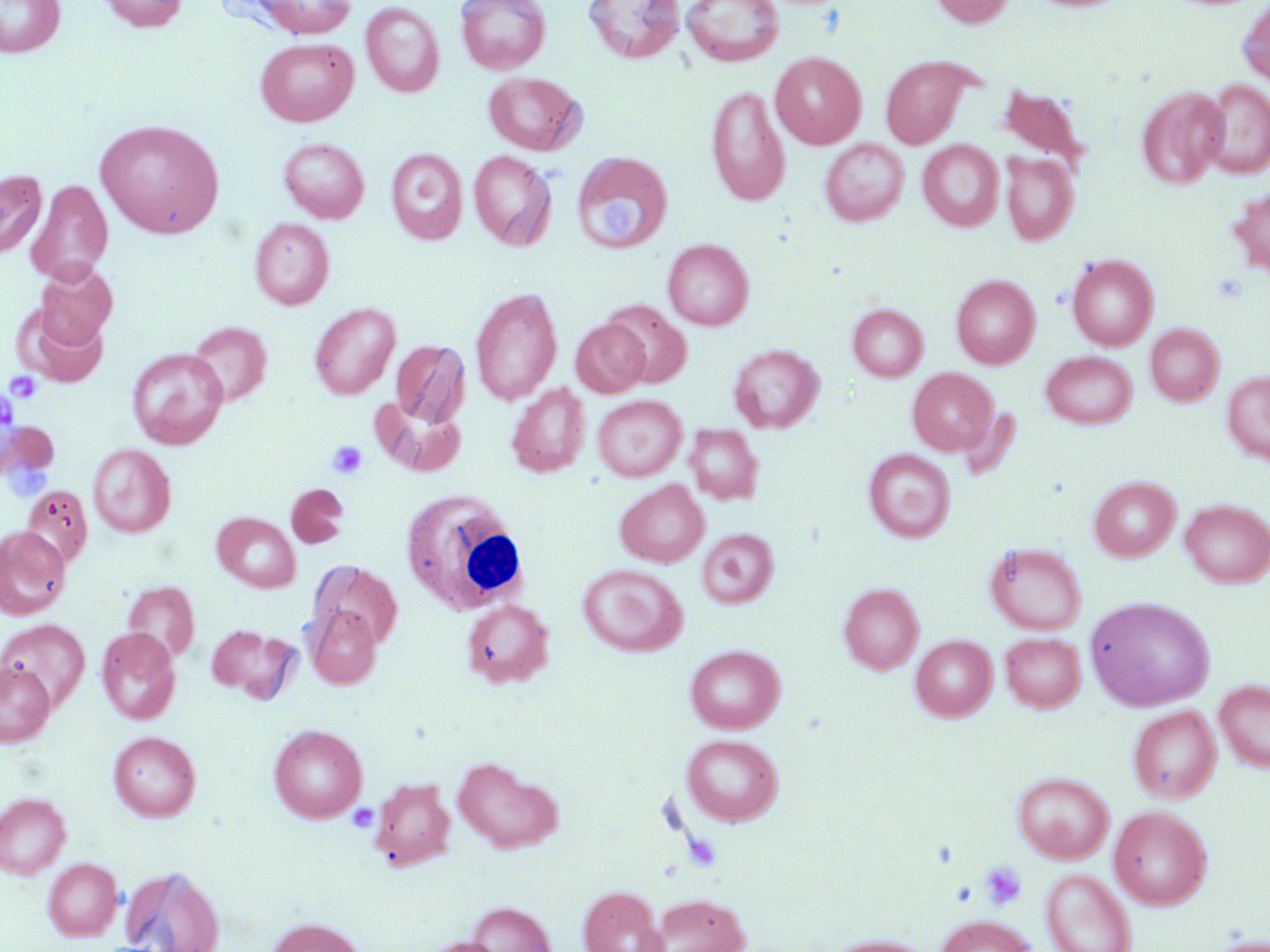
Approximate bounding boxes as (x1, y1, x2, y2) in pixels. Platelet locations (subset): (598, 195, 646, 243), (5, 371, 42, 405), (327, 440, 368, 479), (347, 804, 378, 832), (979, 862, 1026, 911), (950, 882, 976, 907). Uninfected red blood cell locations (subset): (0, 0, 65, 57), (100, 0, 187, 32), (456, 0, 550, 74), (583, 0, 685, 63), (682, 0, 784, 66), (929, 0, 1017, 28), (1029, 0, 1127, 13), (1238, 0, 1270, 90), (251, 1, 358, 38), (361, 1, 444, 97), (255, 38, 358, 126), (771, 51, 866, 149), (881, 54, 976, 149), (482, 71, 586, 155), (1200, 79, 1270, 178), (706, 84, 790, 207), (995, 84, 1090, 171), (1137, 86, 1228, 188), (95, 119, 224, 238), (278, 137, 369, 223), (820, 138, 909, 226), (918, 140, 1003, 231), (385, 148, 468, 244), (469, 150, 556, 250), (571, 152, 673, 255), (1001, 152, 1079, 245), (0, 170, 46, 257), (26, 179, 113, 285), (1227, 186, 1270, 278), (249, 218, 334, 309), (663, 238, 754, 330), (1067, 254, 1158, 351), (33, 263, 117, 350), (951, 274, 1040, 368), (470, 286, 563, 405), (602, 299, 693, 388), (309, 302, 400, 400), (848, 303, 928, 381), (17, 304, 109, 387), (571, 319, 649, 397), (185, 321, 272, 407), (1145, 323, 1224, 406), (390, 339, 470, 430), (728, 343, 825, 433), (127, 347, 228, 449), (1041, 351, 1137, 428), (907, 367, 997, 454), (1222, 371, 1270, 465), (507, 382, 590, 477), (926, 390, 1011, 471), (592, 394, 686, 481), (373, 399, 467, 476), (958, 406, 1021, 481), (684, 424, 764, 505), (88, 443, 176, 537), (864, 449, 955, 542), (1088, 476, 1180, 561), (615, 480, 709, 567), (286, 484, 349, 548), (21, 485, 93, 567), (1180, 499, 1270, 587), (213, 512, 300, 592), (0, 527, 71, 619), (697, 529, 779, 609), (986, 543, 1086, 635), (309, 560, 403, 652), (578, 563, 687, 657), (122, 582, 200, 662), (838, 583, 923, 674), (1084, 595, 1216, 711), (461, 598, 555, 687), (307, 606, 383, 688), (0, 619, 90, 712), (207, 624, 298, 701), (97, 628, 180, 724), (1000, 632, 1085, 712), (911, 635, 997, 721), (685, 644, 784, 733), (0, 661, 54, 747), (1214, 678, 1270, 773), (1128, 705, 1221, 802), (268, 724, 367, 822), (108, 731, 201, 821), (681, 734, 783, 825), (453, 756, 564, 854), (1012, 771, 1114, 863), (370, 777, 455, 870), (0, 792, 71, 878), (1109, 805, 1212, 910), (43, 857, 123, 941), (119, 863, 226, 952), (1041, 868, 1137, 952), (578, 886, 667, 952), (651, 894, 750, 952), (466, 901, 555, 952), (936, 915, 1035, 952), (266, 917, 366, 952), (820, 934, 938, 952), (1205, 934, 1270, 952), (422, 937, 507, 952). White blood cell locations: (402, 488, 532, 617). Slide-level diagnosis: no evidence of blood parasites. Single field of view. Optical microscopy. Image is 1270×952 pixels. May-Grünwald-Giemsa stain. Thin blood smear. 1000x magnification.